Classify this cell by malaria status.
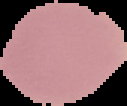
It is uninfected.

image type = cell region segmented out of the field of view; surrounding area masked to black
preparation = thin blood smear
image size = 127×106 pixels